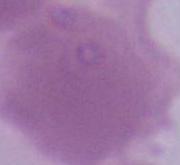
magnification = 1000x
identification = red blood cell
modality = micrograph